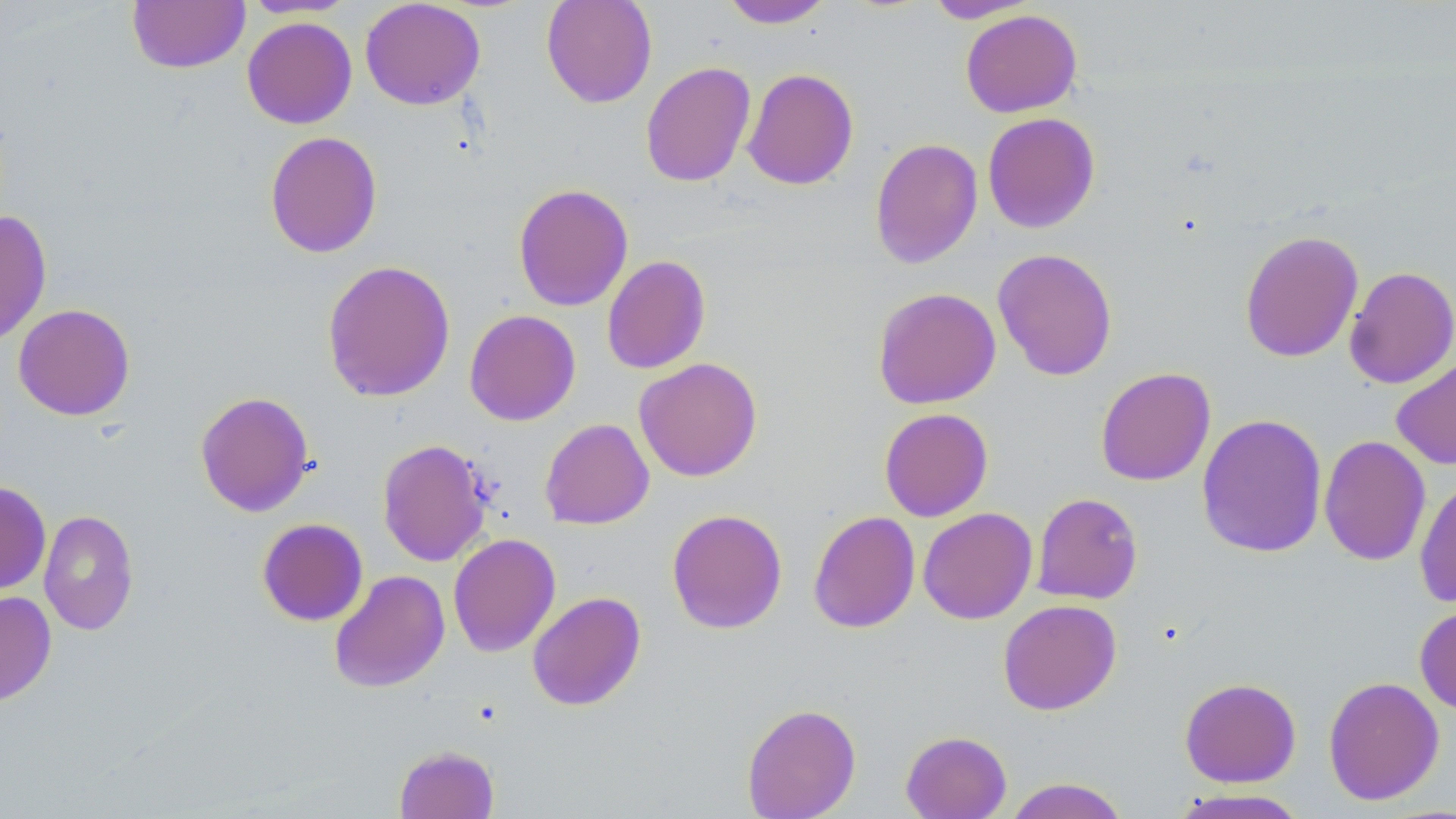
slide-level diagnosis = no evidence of blood parasites
modality = light microscopy
image size = 1456×819 pixels
uninfected red blood cell locations = approximate bounding boxes as (x1, y1, x2, y2) in pixels: (127, 0, 250, 74), (241, 0, 357, 18), (541, 0, 657, 108), (719, 0, 836, 28), (924, 0, 1041, 23), (360, 1, 485, 110), (960, 9, 1082, 118), (242, 16, 357, 129), (640, 61, 756, 187), (742, 68, 859, 190), (982, 112, 1101, 233), (264, 131, 382, 258), (869, 138, 983, 268), (513, 183, 633, 311), (0, 210, 52, 346), (1239, 230, 1363, 363), (992, 248, 1118, 381), (602, 255, 711, 374), (322, 259, 456, 403), (1343, 266, 1456, 389), (872, 287, 1001, 409), (13, 303, 135, 421), (464, 310, 581, 426), (1391, 355, 1456, 470), (634, 357, 762, 482), (1095, 367, 1216, 487), (195, 390, 315, 517), (879, 408, 993, 522), (1197, 413, 1328, 558), (539, 418, 654, 529), (1319, 435, 1431, 566), (377, 439, 491, 567), (1414, 475, 1456, 608), (0, 481, 51, 594), (1032, 492, 1143, 605), (918, 507, 1037, 624), (38, 509, 139, 635), (666, 509, 788, 634), (808, 511, 921, 634), (257, 518, 368, 626), (447, 533, 561, 657), (329, 569, 450, 693), (0, 590, 56, 706), (527, 591, 647, 711), (998, 599, 1122, 715), (1415, 604, 1456, 715), (1323, 676, 1445, 805), (1179, 677, 1301, 787), (742, 702, 861, 819), (900, 730, 1012, 819), (393, 744, 500, 819), (1004, 777, 1130, 819), (1168, 788, 1313, 818)
preparation = thin blood film
field of view = single
stain = May-Grünwald-Giemsa
magnification = 1000x